Locate and identify every blood parasite.
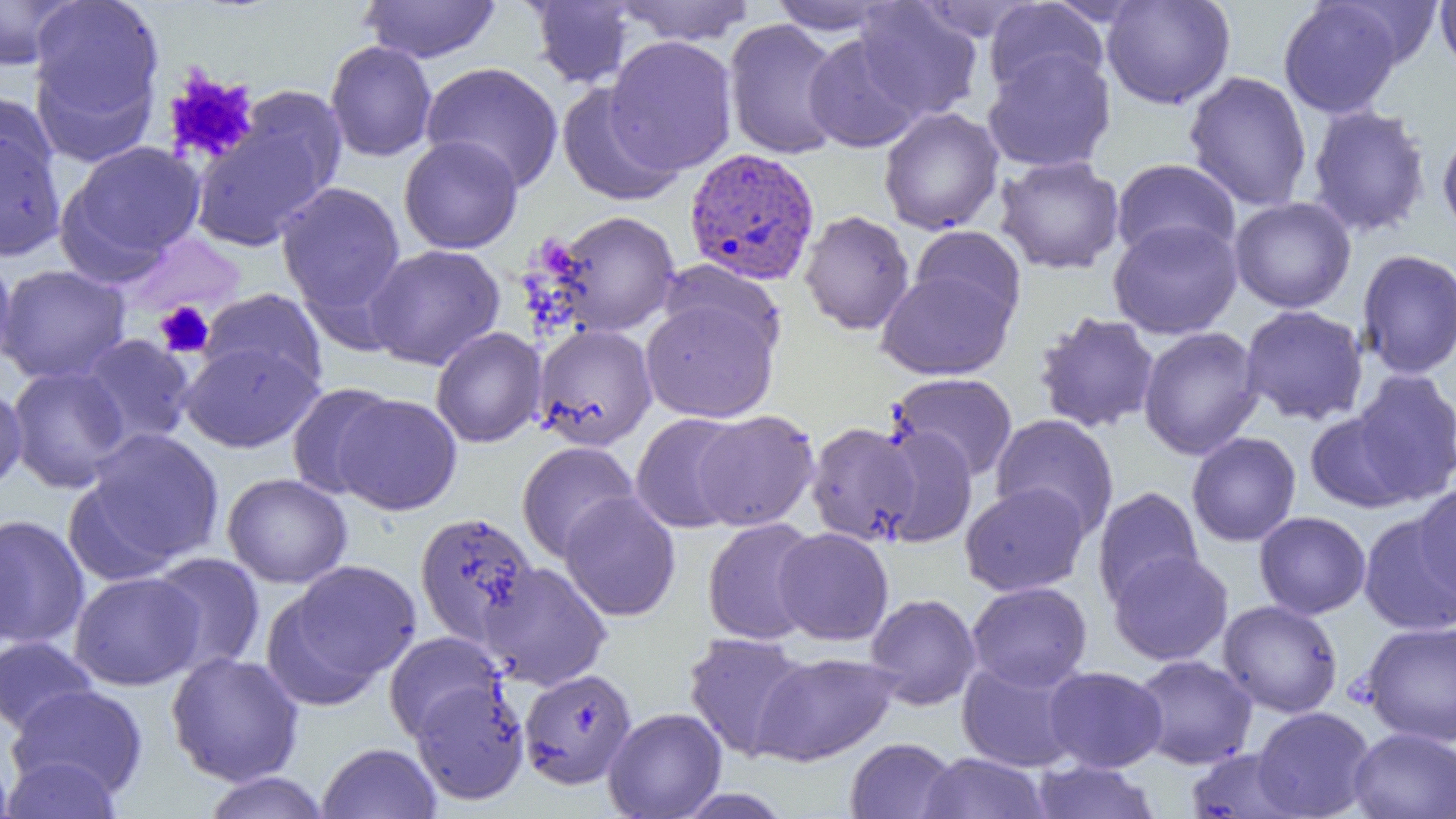
Approximate bounding boxes as (x1, y1, x2, y2) in pixels.
Plasmodium vivax-infected red blood cells: (684, 147, 821, 285).
No Plasmodium falciparum, Plasmodium ovale, Plasmodium malariae, Babesia divergens, or Trypanosoma brucei observed.

Platelet locations: (161, 69, 260, 167), (154, 301, 214, 358). Uninfected red blood cell locations: (0, 0, 79, 71), (359, 0, 501, 64), (613, 0, 757, 45), (766, 0, 898, 35), (1101, 0, 1236, 109), (1434, 0, 1456, 75), (528, 1, 638, 88), (983, 1, 1109, 98), (1330, 1, 1444, 69), (854, 2, 983, 121), (1278, 2, 1404, 119), (30, 5, 166, 144), (723, 18, 847, 160), (604, 34, 739, 175), (804, 34, 925, 153), (325, 40, 438, 162), (982, 49, 1116, 173), (421, 61, 564, 192), (1184, 71, 1313, 211), (557, 84, 684, 206), (236, 85, 347, 202), (0, 91, 59, 195), (1306, 104, 1432, 238), (878, 106, 1004, 235), (190, 115, 334, 252), (0, 123, 67, 262), (1437, 124, 1456, 244), (398, 135, 523, 254), (62, 141, 207, 269), (994, 155, 1125, 275), (1111, 158, 1241, 262), (276, 182, 406, 315), (1229, 196, 1357, 314), (549, 210, 681, 336), (799, 210, 915, 335), (1107, 218, 1243, 340), (909, 226, 1026, 328), (365, 244, 505, 370), (0, 246, 17, 375), (1356, 249, 1456, 380), (658, 260, 785, 360), (0, 264, 131, 384), (876, 268, 1016, 380), (198, 288, 327, 392), (640, 297, 780, 423), (1240, 305, 1369, 425), (1033, 312, 1161, 434), (532, 324, 658, 450), (1137, 326, 1265, 461), (430, 327, 546, 448), (76, 334, 197, 450), (179, 341, 323, 453), (7, 364, 131, 493), (1350, 369, 1456, 504), (889, 373, 1018, 482), (0, 380, 28, 494), (286, 382, 398, 499), (332, 393, 463, 515), (692, 410, 819, 531), (1305, 411, 1417, 513), (630, 413, 749, 533), (990, 414, 1119, 537), (805, 421, 922, 546), (872, 426, 979, 546), (80, 428, 225, 569), (1187, 432, 1301, 547), (516, 441, 640, 562), (222, 473, 353, 588), (960, 482, 1090, 596), (1413, 483, 1456, 603), (1092, 487, 1204, 608), (559, 492, 681, 621), (415, 511, 539, 646), (1254, 511, 1372, 619), (0, 514, 90, 650), (1356, 514, 1456, 637), (702, 517, 821, 645), (0, 521, 22, 651), (772, 528, 894, 646), (1108, 550, 1233, 666), (148, 552, 266, 675), (276, 560, 421, 700), (479, 562, 612, 690), (69, 571, 205, 691), (966, 581, 1093, 691), (865, 593, 981, 710), (1218, 600, 1343, 718), (1361, 621, 1456, 747), (383, 632, 507, 743), (683, 632, 812, 760), (0, 635, 99, 736), (166, 651, 305, 786), (751, 651, 900, 766), (1131, 654, 1258, 769), (957, 657, 1085, 772), (1043, 666, 1167, 772), (519, 668, 637, 789), (407, 682, 531, 807), (7, 685, 148, 798), (1251, 706, 1376, 819), (603, 707, 727, 819), (1348, 727, 1456, 819), (844, 737, 960, 819), (317, 742, 442, 819), (1184, 746, 1304, 819), (0, 748, 15, 819), (918, 752, 1051, 818), (0, 755, 124, 818), (1030, 759, 1161, 818), (201, 771, 332, 819), (672, 788, 794, 818). Slide-level diagnosis: Plasmodium vivax. Image is 1456×819 pixels. Thin blood smear. Single field of view. Captured at 1000x magnification. Light microscopy.